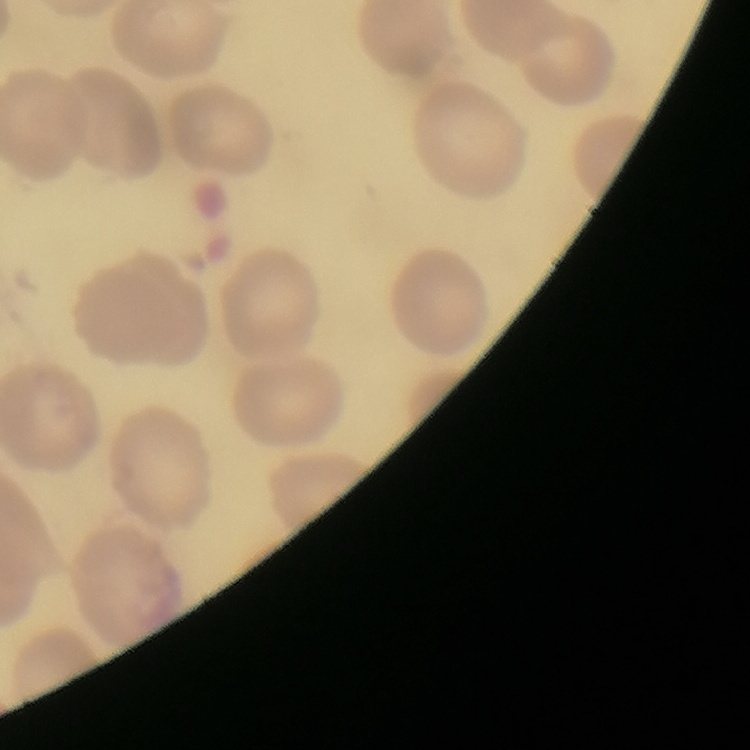
Summary:
  - Erythrocyte morphology: no rouleaux formation
  - Stain: Field's or Giemsa
  - Image type: one tile cut from a larger photomicrograph
  - Preparation: thin blood smear